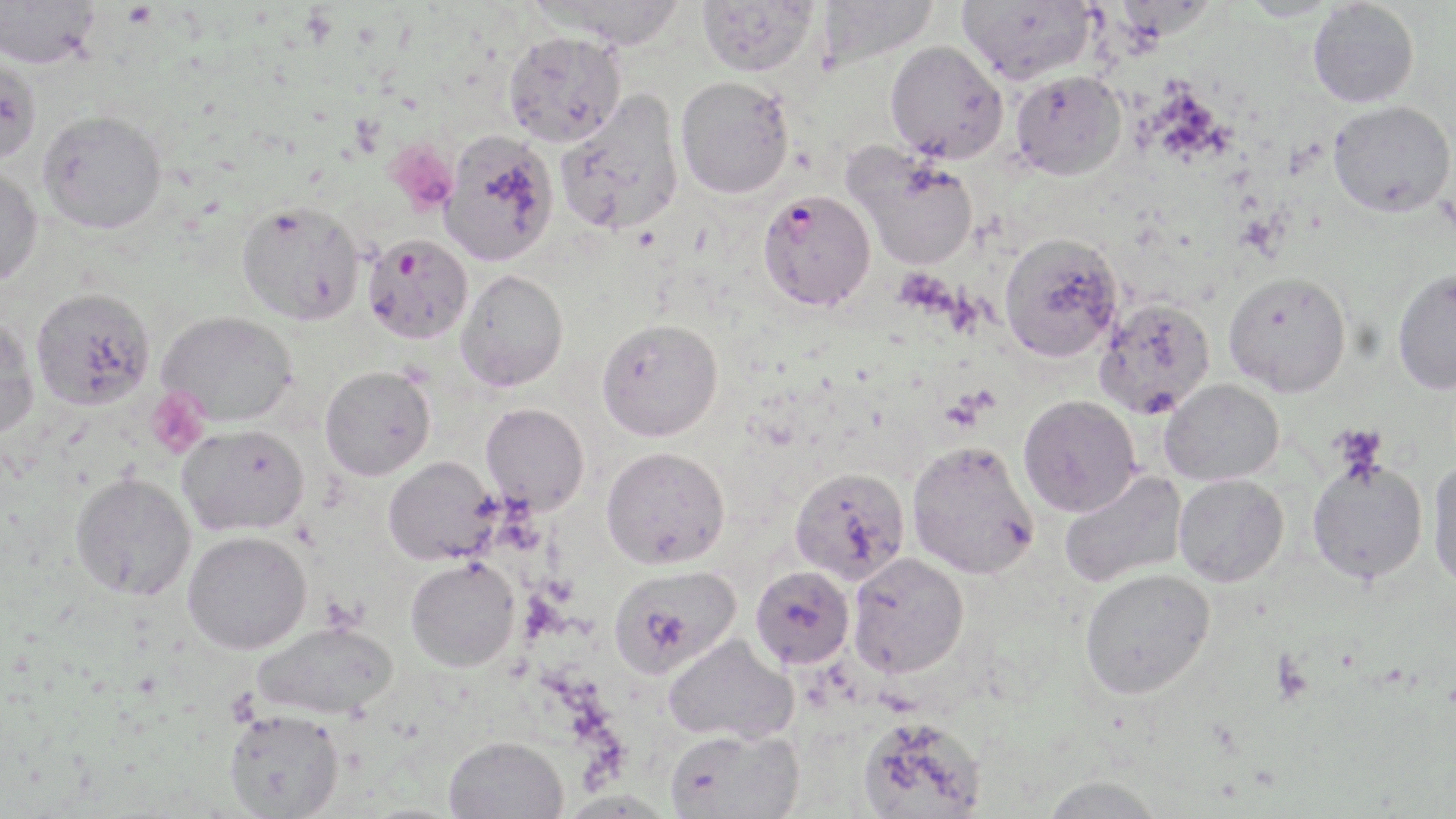 Approximate bounding boxes as (x1, y1, x2, y2) in pixels. Plasmodium falciparum-infected red blood cell locations: (757, 189, 876, 312), (362, 233, 473, 344). Platelet locations: (386, 140, 458, 216), (145, 387, 209, 458), (1331, 426, 1387, 475), (1271, 653, 1312, 705). Uninfected red blood cell locations: (0, 0, 100, 72), (526, 0, 690, 53), (697, 0, 817, 80), (816, 0, 940, 71), (958, 0, 1096, 84), (1238, 0, 1341, 21), (1308, 1, 1419, 108), (503, 35, 627, 150), (885, 41, 1008, 166), (0, 60, 42, 167), (1011, 70, 1127, 179), (675, 78, 794, 201), (555, 90, 685, 238), (1328, 100, 1455, 217), (38, 113, 166, 237), (438, 132, 559, 267), (844, 145, 978, 270), (0, 167, 44, 288), (236, 201, 365, 326), (999, 232, 1123, 362), (1392, 268, 1456, 395), (456, 269, 568, 391), (1223, 270, 1352, 396), (32, 289, 155, 413), (1095, 297, 1215, 419), (158, 311, 297, 428), (0, 315, 39, 440), (596, 318, 723, 441), (319, 365, 435, 480), (1160, 379, 1284, 486), (1019, 395, 1141, 516), (481, 403, 589, 514), (177, 425, 309, 536), (906, 439, 1040, 579), (601, 446, 730, 569), (383, 457, 500, 565), (1307, 458, 1428, 583), (1426, 459, 1456, 593), (789, 467, 910, 585), (1059, 469, 1187, 588), (69, 473, 196, 602), (1174, 474, 1289, 587), (182, 531, 312, 656), (847, 552, 969, 678), (405, 559, 520, 671), (608, 564, 741, 677), (750, 565, 854, 668), (1079, 567, 1215, 698), (252, 622, 397, 720), (663, 633, 798, 744), (223, 709, 344, 818), (856, 715, 987, 818), (665, 727, 804, 819), (444, 735, 568, 819), (1038, 775, 1166, 819). Slide-level diagnosis: Plasmodium falciparum. Optical microscopy. Thin blood film. May-Grünwald-Giemsa stain. Single field of view. Captured at 1000x magnification. Image is 1456×819 pixels.